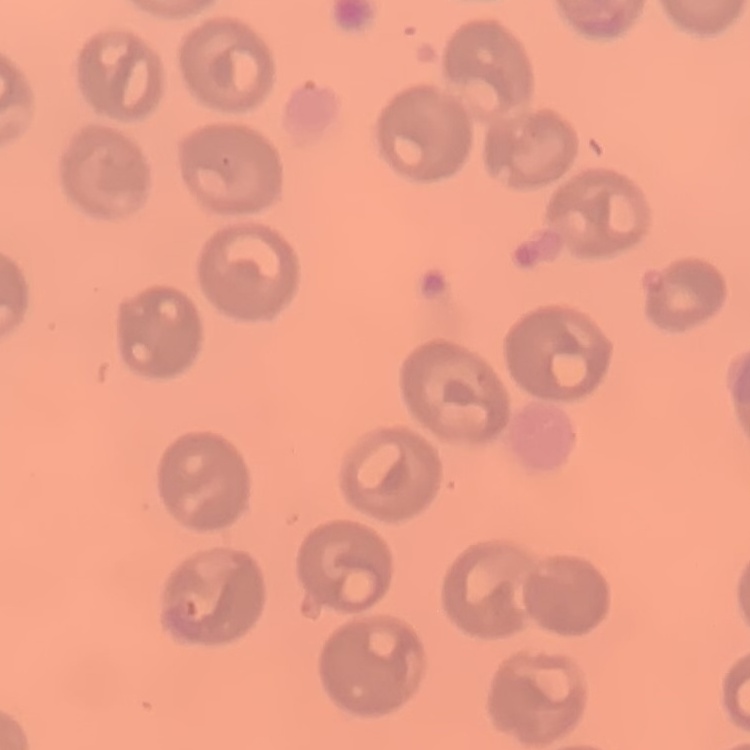

Summary:
  - Erythrocyte morphology: no rouleaux formation
  - Stain: Field's or Giemsa
  - Preparation: thin blood smear
  - Image type: one tile cut from a larger photomicrograph